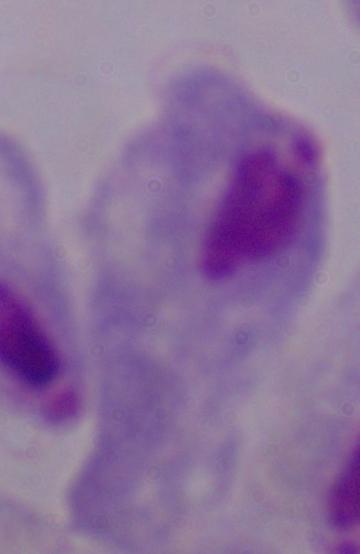

1000x magnification. Photomicrograph. A trichomonad is shown.